Assess the morphology of the red blood cells.
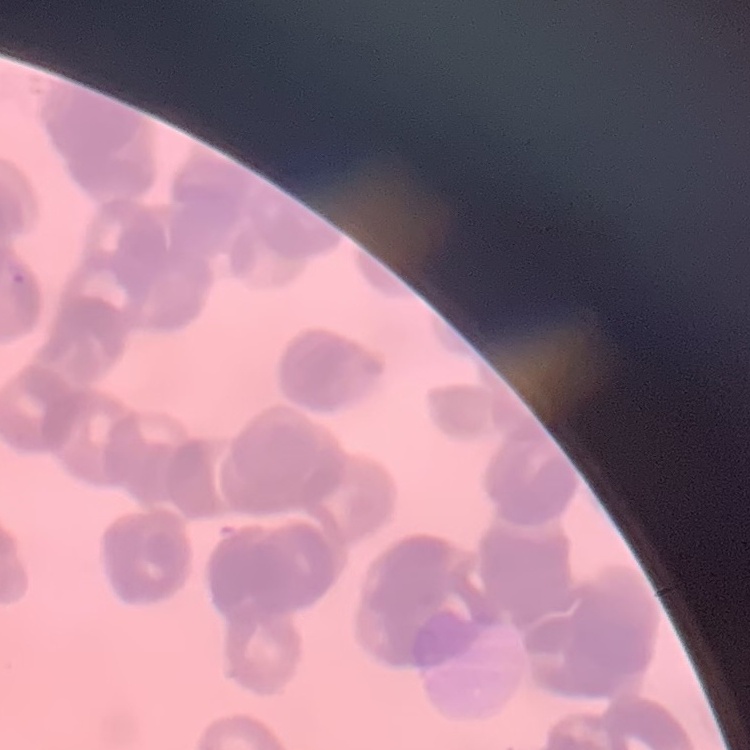

Rouleaux formation.

One tile cut from a larger photomicrograph. Field's or Giemsa stain. Thin blood smear.